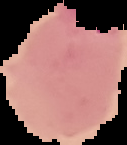
Image is 127×145 pixels. Segmented cell region on a black background. From a thin blood smear. Result: Plasmodium parasites identified.